Identify the parasite.
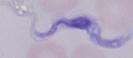
This is a trypanosome.

modality = micrograph
magnification = 1000x